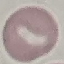

result = negative for malaria parasites
stain = Giemsa
capture = smartphone camera at the microscope eyepiece
image type = cell patch, automatically extracted from a larger field of view and resized to 64 × 64 pixels
preparation = thin blood smear